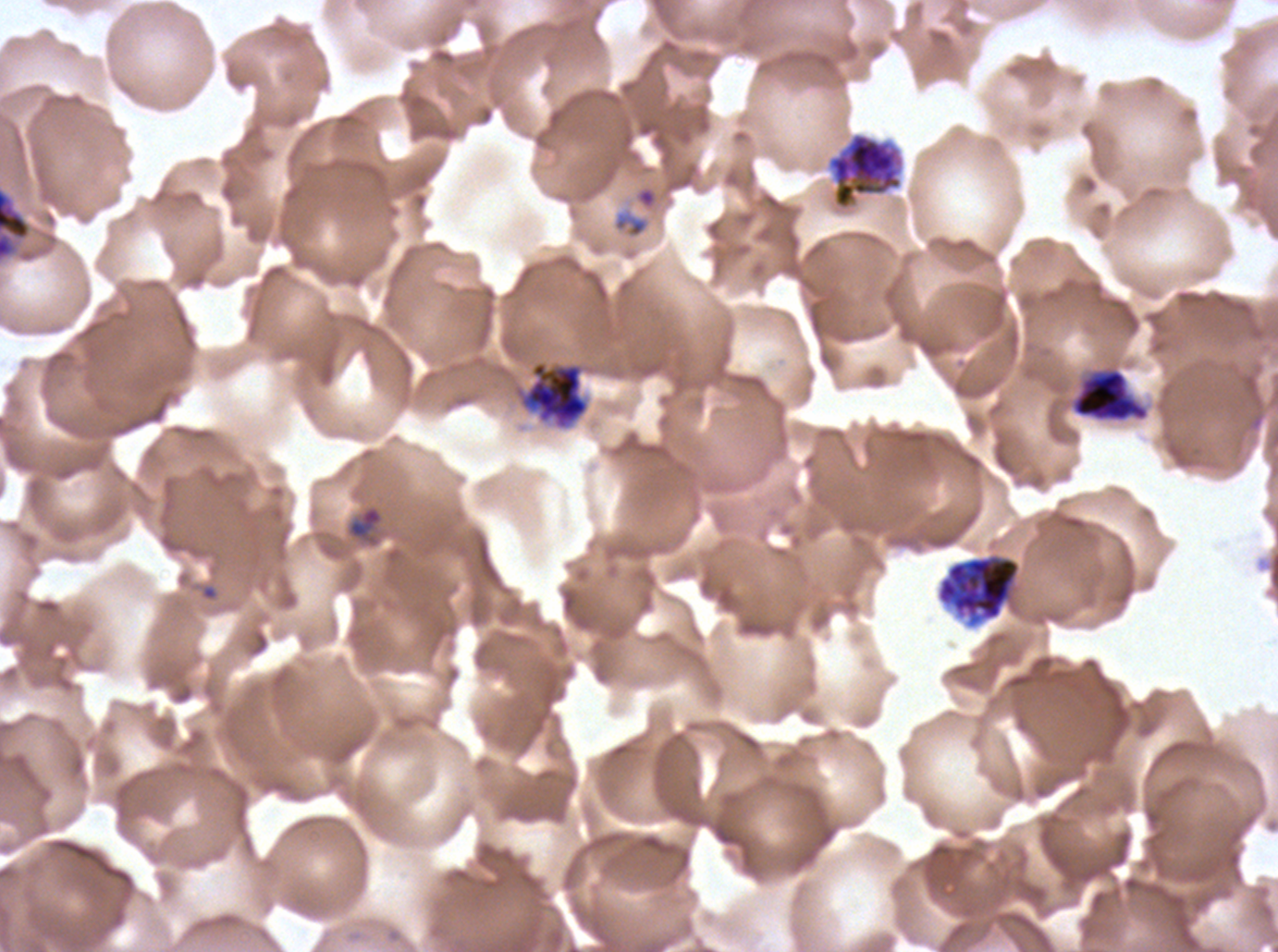

Approximate bounding boxes as {x1, y1, x2, y2} in pixels. Early schizont locations: {827, 132, 903, 210}, {0, 186, 32, 263}, {520, 360, 589, 429}, {1071, 368, 1149, 422}. Ring locations: {347, 505, 384, 542}. Segmenter locations: {936, 552, 1022, 629}. Plasmodium falciparum cultured ex vivo for 24 to 48 hours, from a patient in The Gambia. One sub-image of a larger composite. Giemsa stain. Thin blood smear. Image is 1278×952 pixels. Life-cycle stages observed: ring, early schizont, segmenter.